Describe the morphology of the red blood cells.
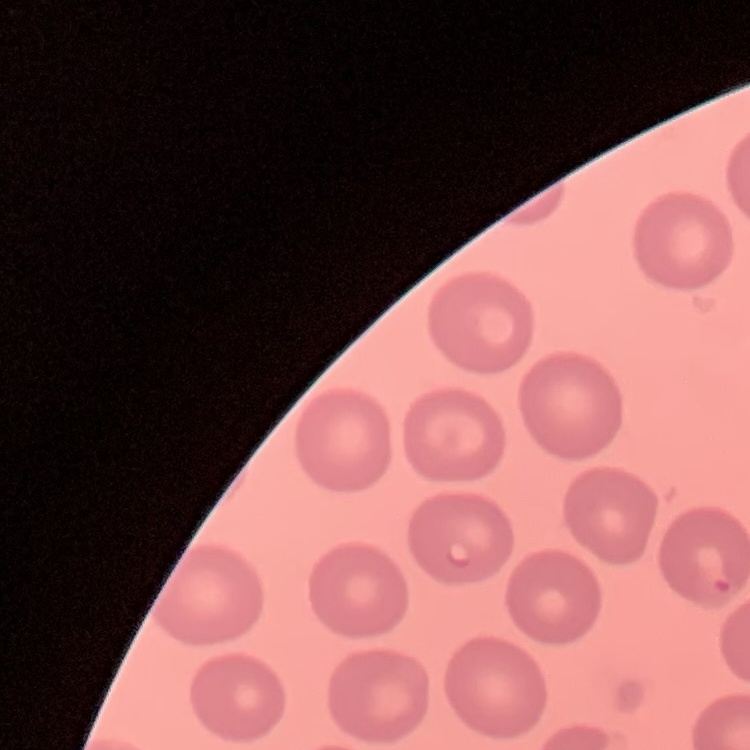

No rouleaux formation.

Field's or Giemsa stain. Thin blood smear. One tile cut from a larger photomicrograph.